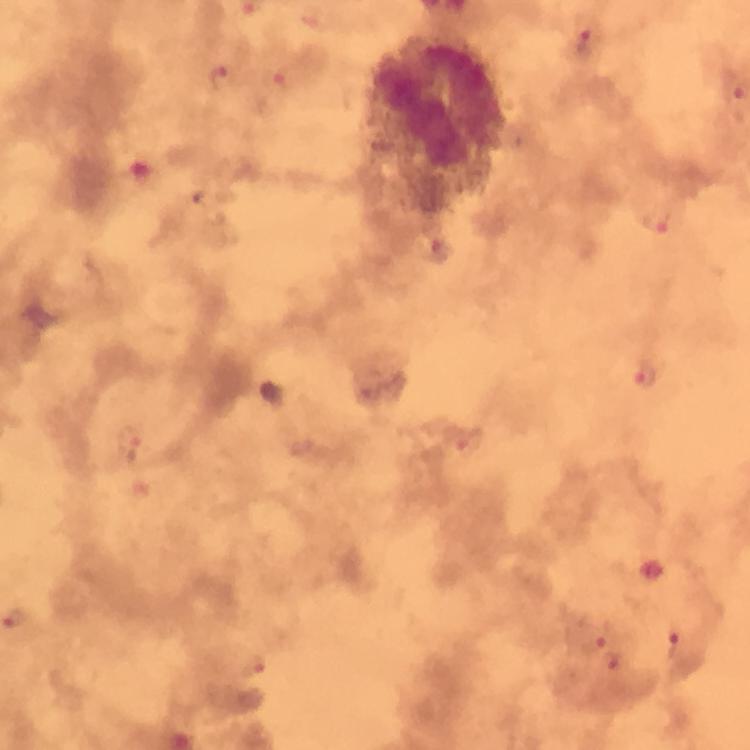

context = from a diagnostic examination for malaria
image size = 750×750 pixels
preparation = thick blood film
malaria parasite locations = approximate centers as [x, y] in pixels: [585, 41], [220, 77], [275, 83], [658, 222], [645, 376], [131, 436], [464, 442], [596, 639], [672, 646], [254, 665], [618, 665]
cropped from = a single field of view
capture = smartphone camera through the microscope
stain = Giemsa
immersion oil = applied
magnification = 100x